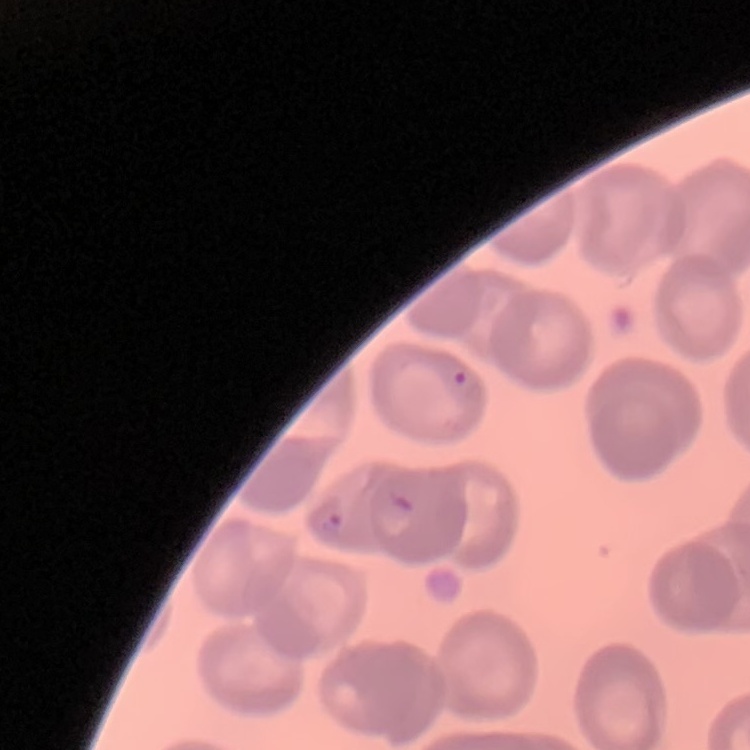

{
  "erythrocyte_morphology": "no rouleaux formation",
  "stain": "Field's or Giemsa",
  "image_type": "square crop of a larger photomicrograph",
  "preparation": "thin peripheral smear"
}